State which cell type is depicted.
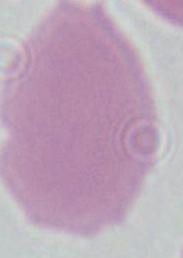

This is an erythrocyte.

Summary:
  - Magnification: 1000x
  - Modality: photomicrograph